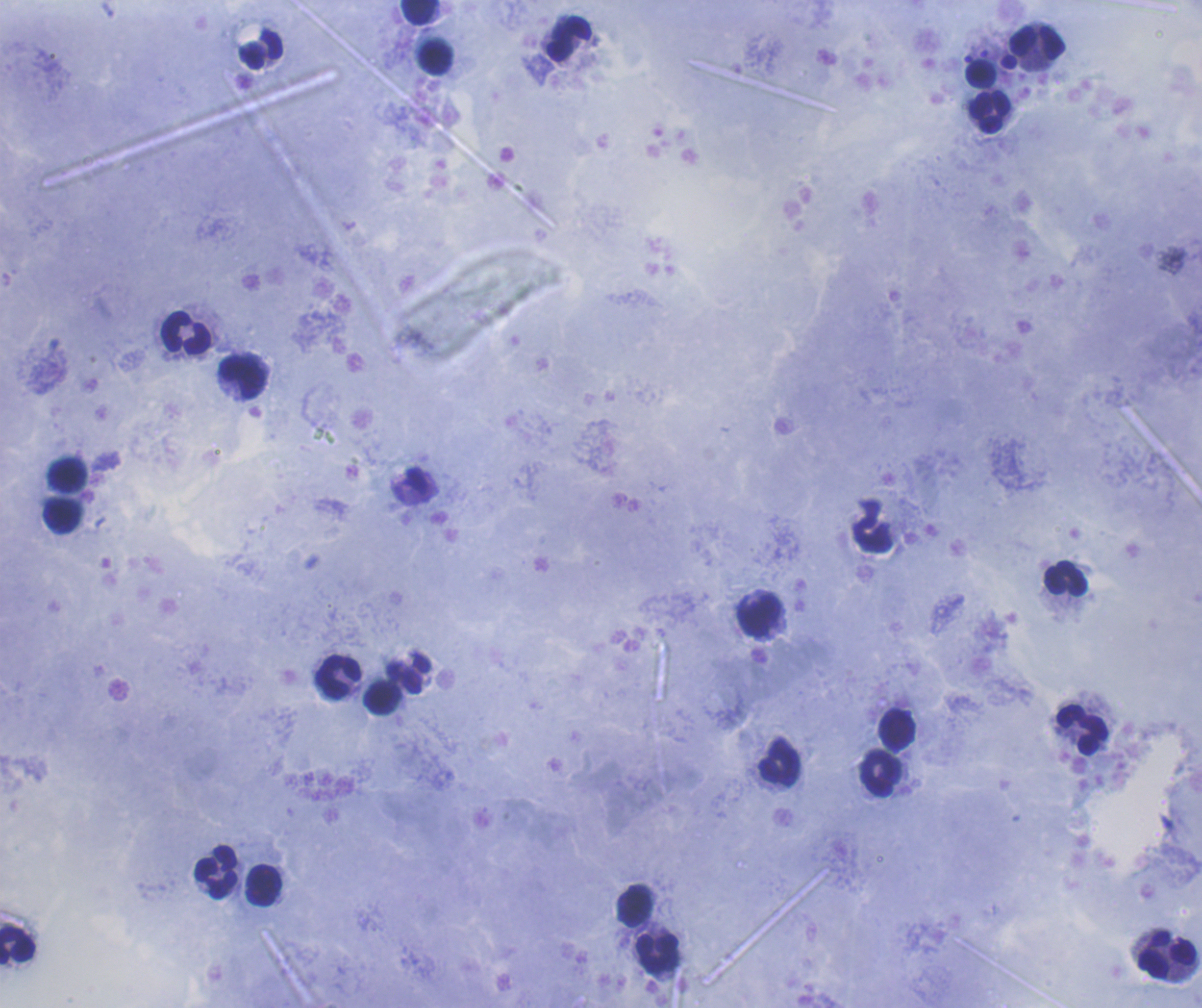
image_size: 1202×1008 pixels
leukocyte_locations: 'approximate centers as {x, y} in pixels: {419, 12}, {569, 39}, {1037, 42}, {260, 50}, {436, 58}, {990, 112}, {186, 333}, {244, 377}, {68, 475}, {62, 516}, {872, 532}, {1066, 578}, {759, 615}, {409, 675}, {339, 676}, {383, 697}, {897, 729}, {1082, 730}, {779, 762}, {882, 773}, {216, 871}, {263, 885}, {634, 905}, {17, 944}, {658, 953}, {1167, 956}'
magnification: 100x
stain: Romanowsky
context: previously used in an actual diagnosis
background_quality: satisfactory
coloration_quality: good
preparation: thick smear of blood
result: no malaria parasites seen
field_of_view: one from this slide